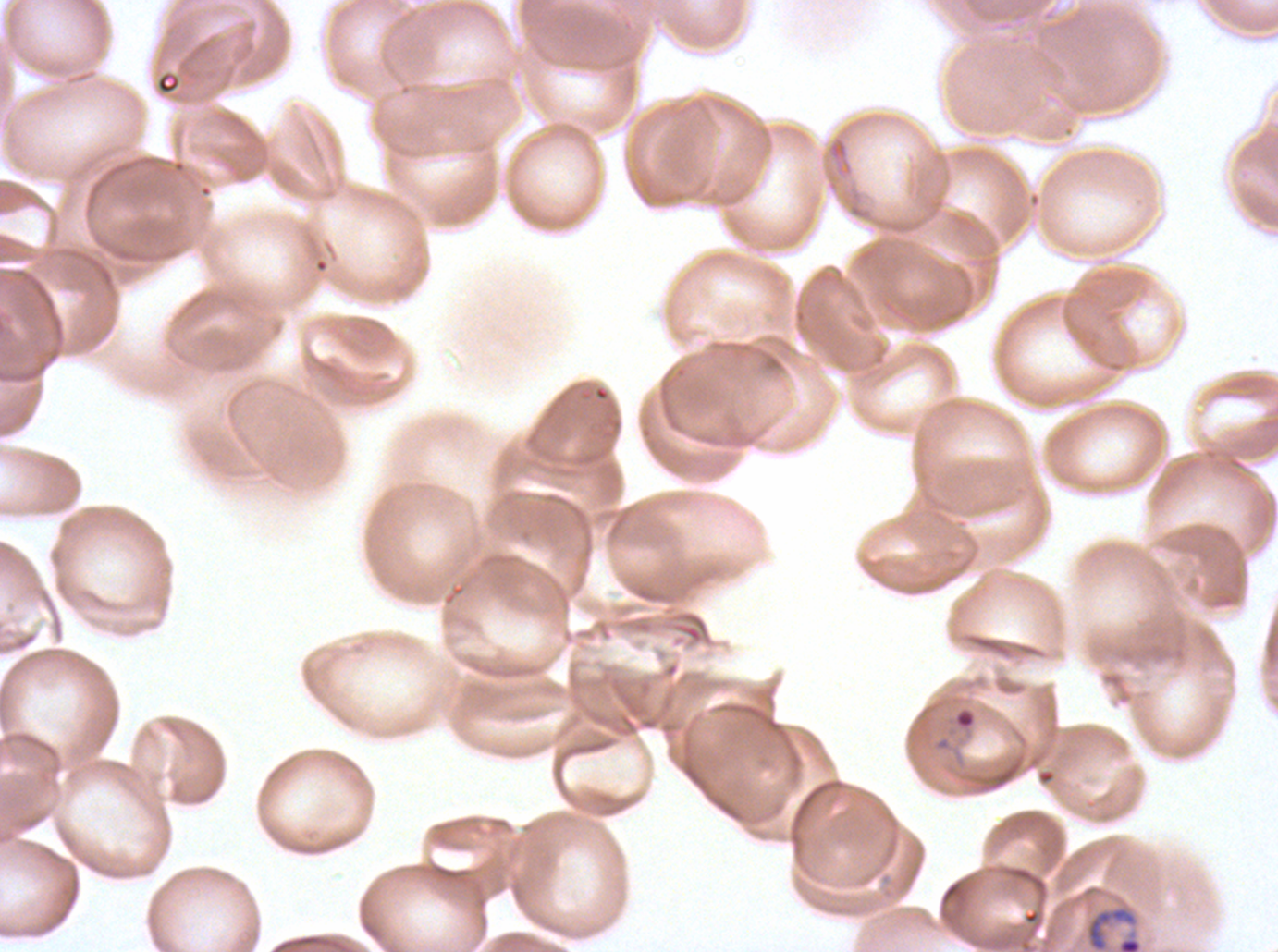

field_of_view: one sub-image of a larger composite
ring_locations: 'approximate bounding boxes as [x1, y1, x2, y2] in pixels: [931, 704, 978, 753], [1086, 907, 1137, 951]'
specimen: ex-vivo P. falciparum culture from a patient in The Gambia, grown for 24 to 48 hours
stain: Giemsa
preparation: thin blood smear
image_size: 1278×952 pixels